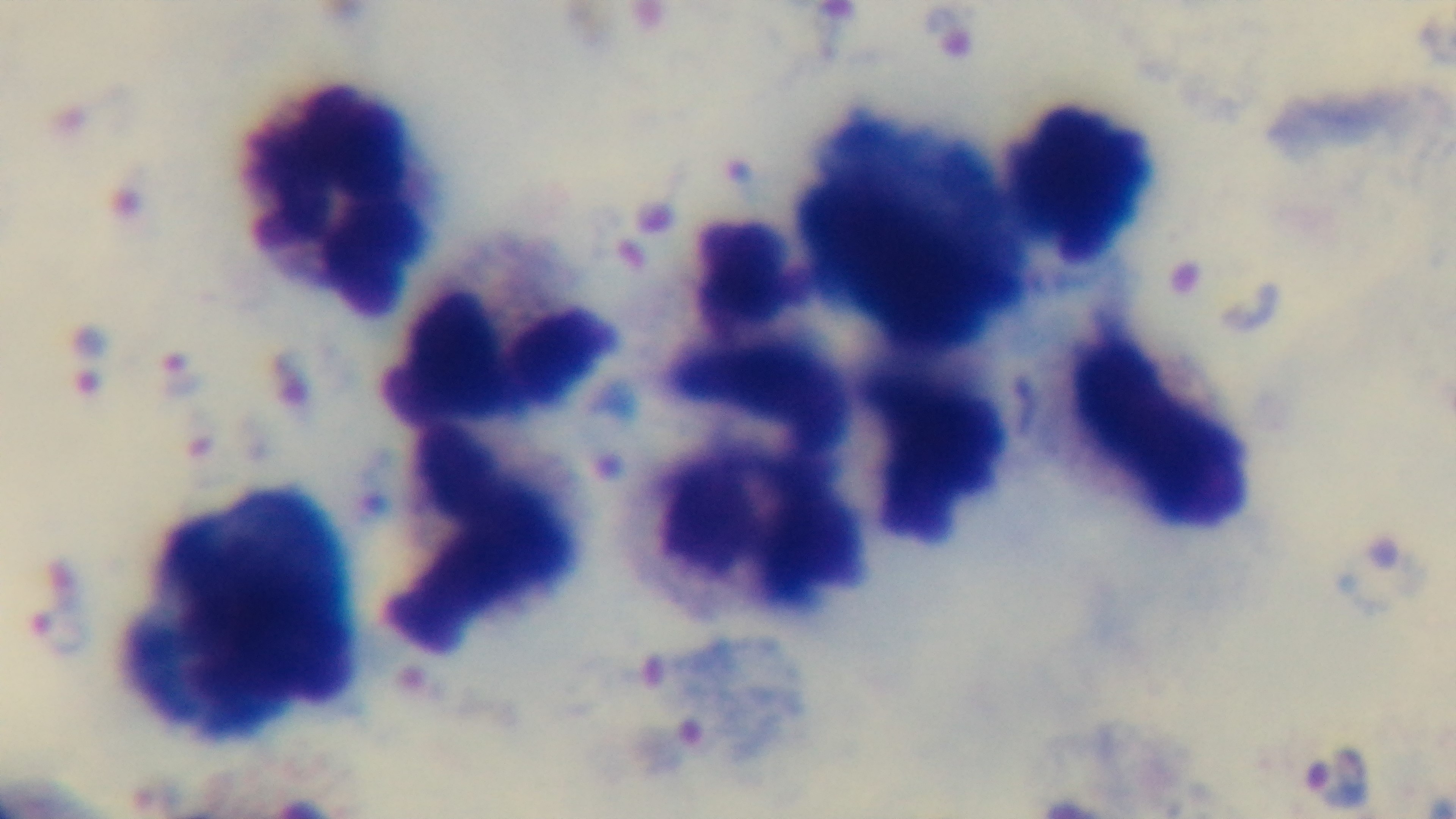

Summary:
  - Objective: 100x oil immersion
  - Modality: light microscopy
  - Capture: mounted 4K digital camera
  - Field of view: one from the slide
  - Preparation: thick
  - Stain: Giemsa
  - Malaria status: infected